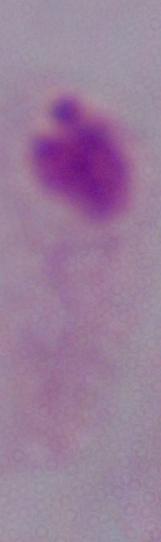
Summary:
  - Modality: micrograph
  - Identification: trichomonad
  - Magnification: 1000x